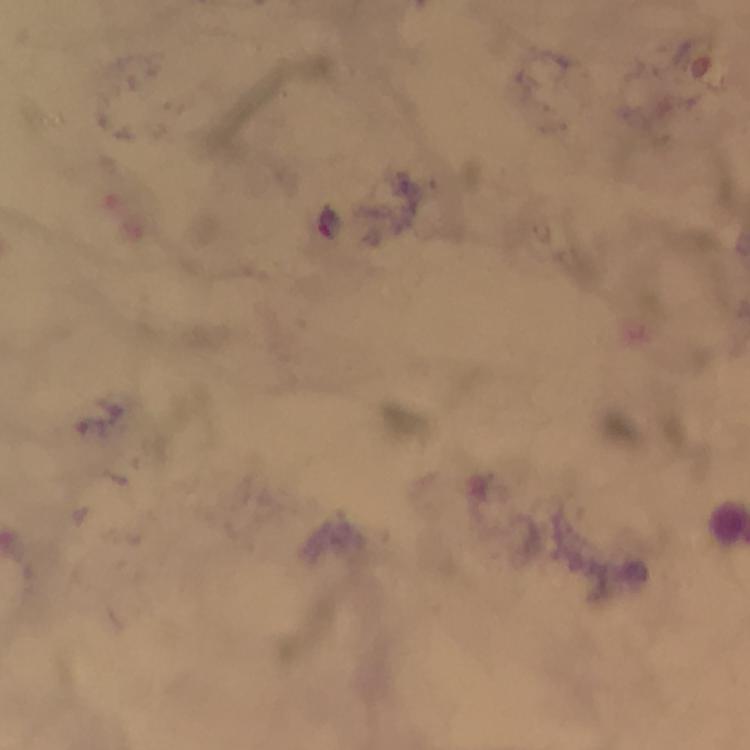

Approximate centers as [x, y] in pixels. Malaria parasite locations: [329, 221]. Cropped region of a single field of view. Thick blood smear. From a malaria diagnostic workup. Image is 750×750 pixels. Immersion oil applied. Smartphone photograph taken through a microscope. At 100x magnification. Giemsa stain.